Identify the parasite.
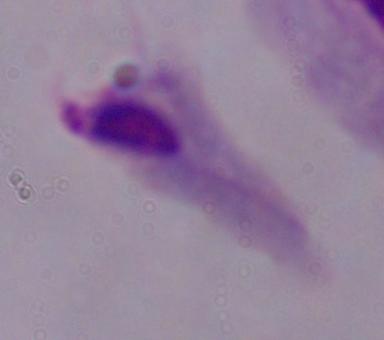

A trichomonad.

Micrograph. Captured at 1000x magnification.